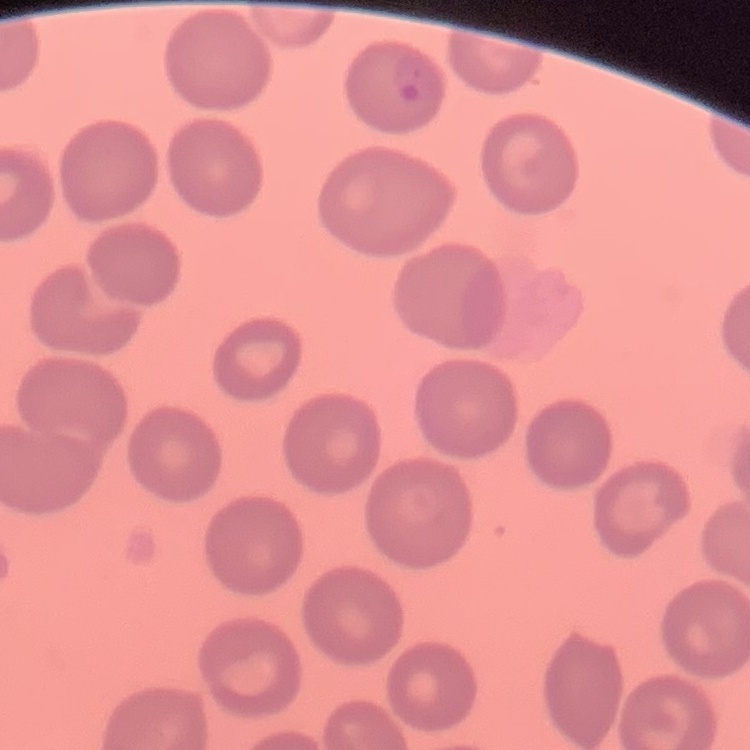

Summary:
  - Red blood cell morphology: no rouleaux formation
  - Preparation: thin blood film
  - Image type: one tile cut from a larger photomicrograph
  - Stain: Field's or Giemsa